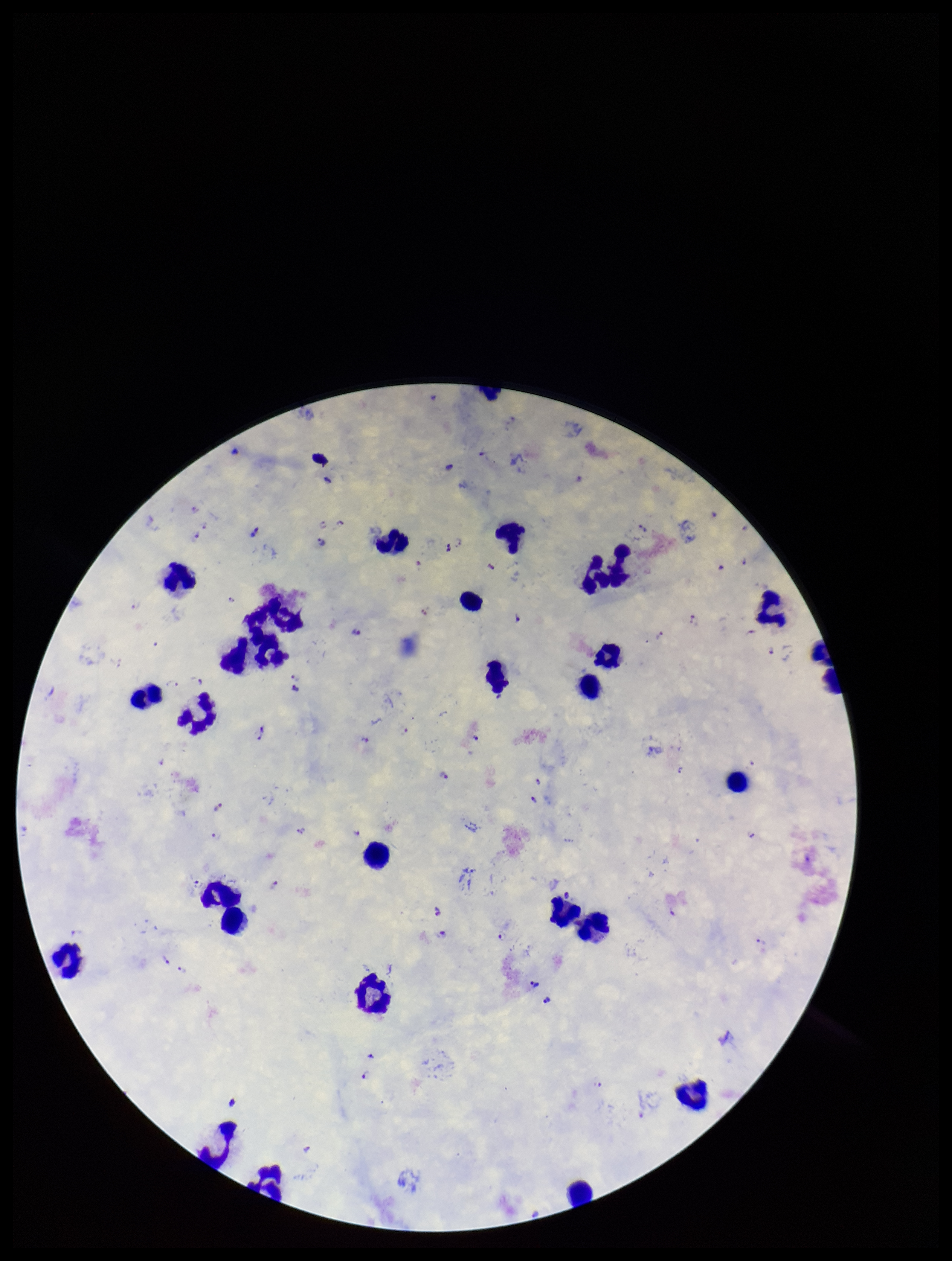

Species reported for this patient: Plasmodium falciparum. Leukocyte count: 26. Parasite count: 49. Patient malaria status: positive. Preparation: thick smear. Image is 952×1261 pixels. Plasmodium parasites: identified. Single field of view. Smartphone photograph taken through the eyepiece of a microscope. Giemsa stain.